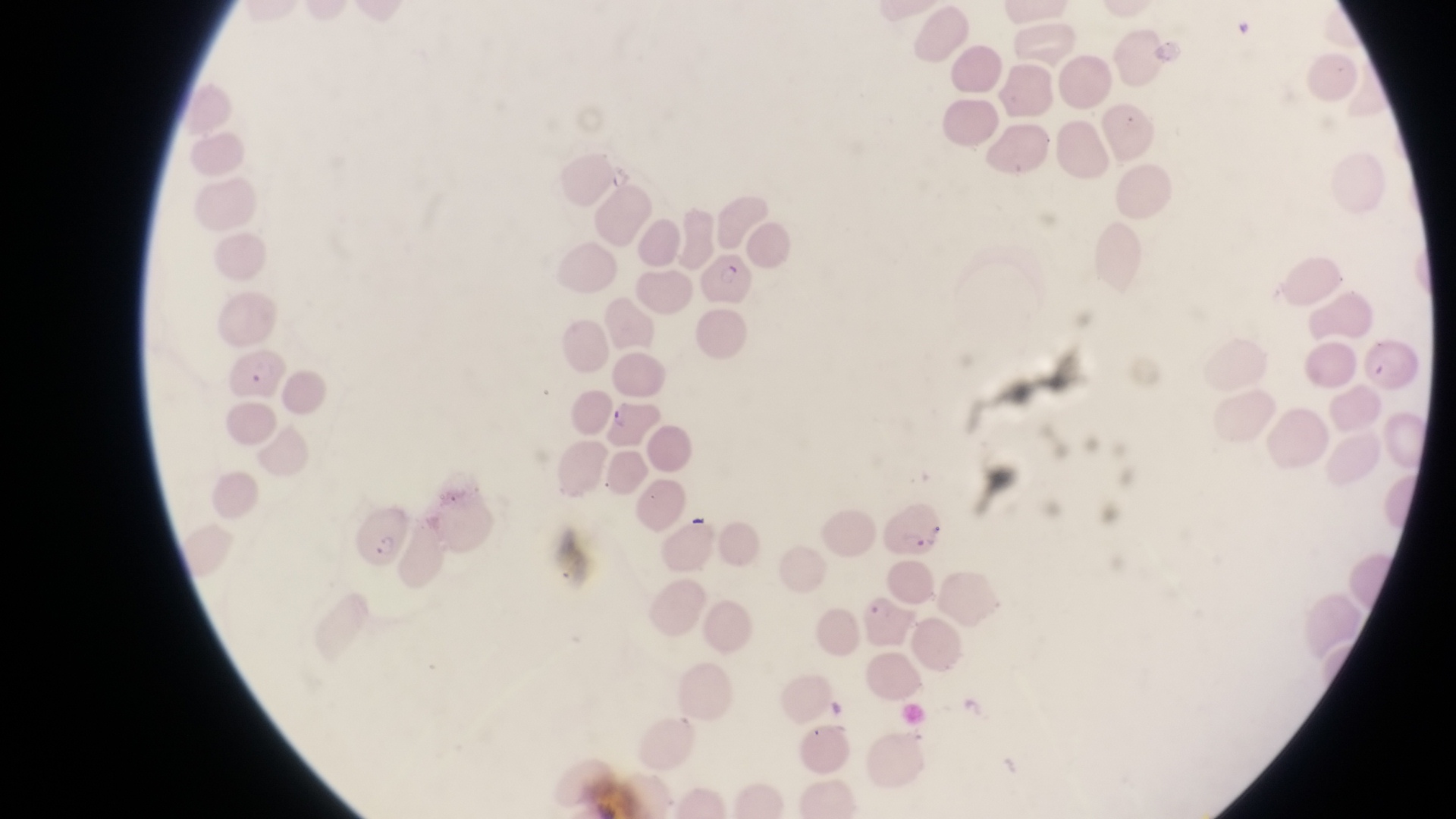

image size = 1456×819 pixels
capture = smartphone photograph through the eyepiece of an Olympus CX-23 microscope
preparation = thin blood smear
magnification = 1000x
parasitised red blood cell locations = approximate bounding boxes as {left, top, right, bottom} in pixels: {698, 245, 754, 309}, {224, 349, 283, 407}, {346, 499, 413, 571}, {881, 501, 949, 560}
country = Uganda
field of view = single